Identify the parasite.
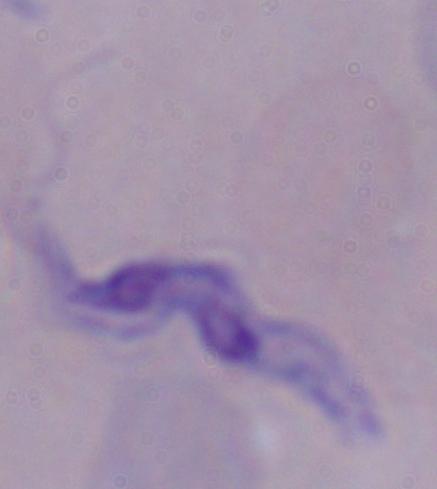

A trypanosome.

Summary:
  - Magnification: 1000x
  - Modality: micrograph